Give the position of every Plasmodium parasite.
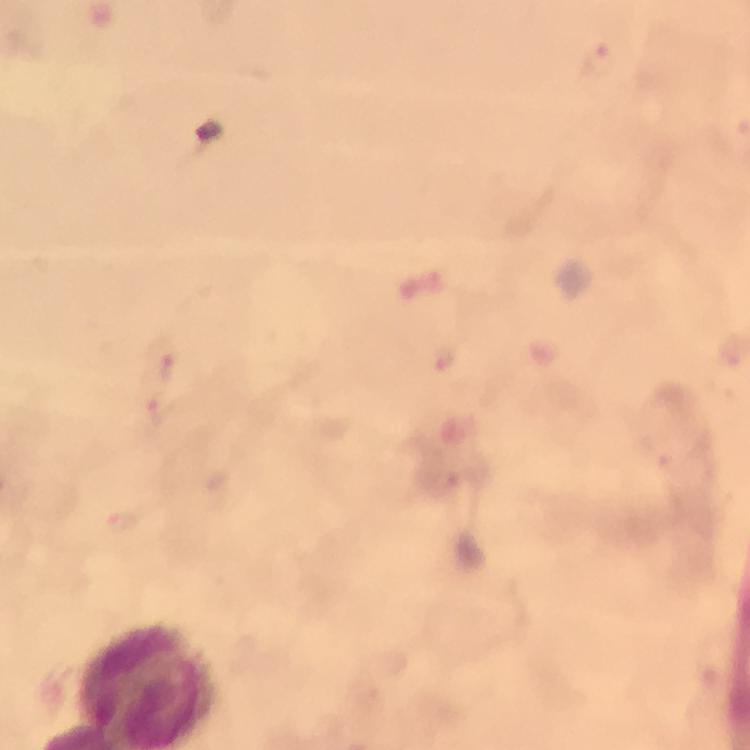

Approximate centers as {x, y} in pixels.
Plasmodium parasites: {602, 61}, {446, 360}, {166, 363}, {161, 407}, {124, 521}.

Smartphone photograph taken through a microscope. At 100x magnification. From a malaria diagnostic workup. Thick blood smear. Image is 750×750 pixels. Giemsa stain. A crop from one field of view. Immersion oil was used.